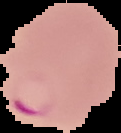
Image is 121×133 pixels. Result: Plasmodium parasites detected. The area outside the segmented cell region is set to black. From a thin blood smear.